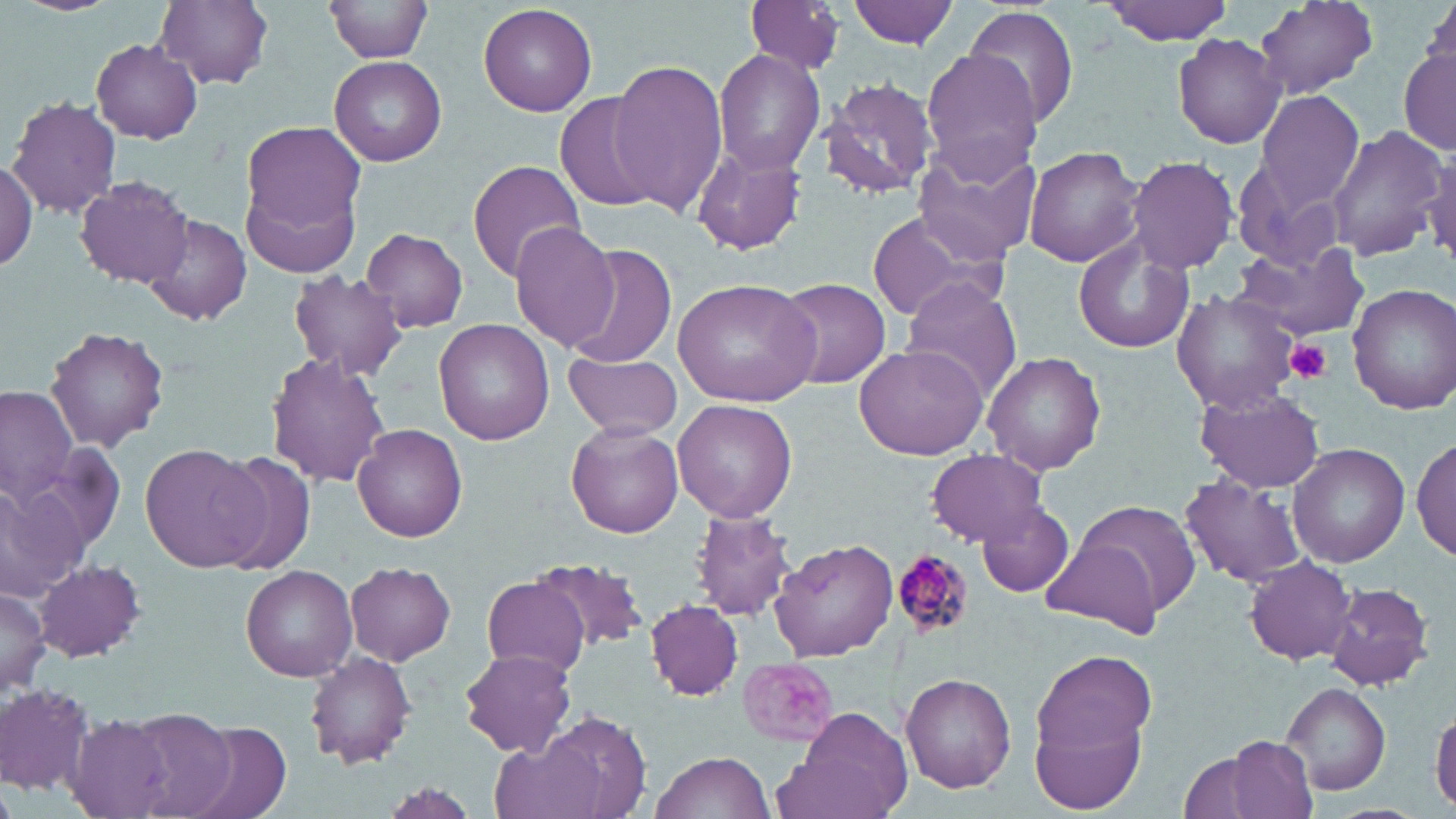
slide-level diagnosis = Plasmodium malariae
magnification = 1000x
preparation = thin blood smear
modality = optical microscopy
field of view = single
platelet locations = approximate bounding boxes as (x1,y1)-(x2,y2) corner pairs in pixels: (1286,339)-(1330,383)
image size = 1456×819 pixels
uninfected red blood cell locations = approximate bounding boxes as (x1,y1)-(x2,y2) corner pairs in pixels: (154,0)-(275,89), (325,0)-(432,63), (848,0)-(958,47), (1101,0)-(1239,44), (1252,0)-(1378,99), (1420,0)-(1456,90), (742,2)-(845,75), (479,3)-(598,116), (963,5)-(1080,130), (1172,34)-(1285,148), (90,39)-(203,143), (1399,47)-(1455,156), (712,49)-(826,176), (921,49)-(1044,180), (329,56)-(447,165), (608,60)-(727,214), (822,77)-(938,199), (1256,89)-(1366,210), (554,91)-(663,214), (7,96)-(121,219), (1327,124)-(1446,261), (239,125)-(365,275), (691,143)-(808,256), (1024,144)-(1145,267), (1422,144)-(1456,269), (911,147)-(1041,267), (1126,155)-(1239,274), (0,158)-(37,271), (468,159)-(586,282), (75,175)-(194,287), (864,211)-(1006,325), (144,213)-(251,326), (508,222)-(621,352), (362,227)-(467,332), (1072,239)-(1195,354), (1233,241)-(1371,342), (568,246)-(676,368), (288,269)-(406,382), (672,278)-(820,407), (771,278)-(891,390), (899,279)-(1022,400), (1348,283)-(1456,414), (1171,289)-(1300,414), (434,318)-(556,444), (45,324)-(169,451), (855,344)-(988,460), (565,350)-(684,442), (984,351)-(1106,475), (266,353)-(390,488), (1,386)-(76,510), (1197,389)-(1324,493), (674,399)-(797,521), (565,422)-(683,538), (353,423)-(467,544), (1412,436)-(1455,561), (141,442)-(265,571), (1288,444)-(1409,568), (925,451)-(1048,546), (209,452)-(319,571), (1180,471)-(1311,587), (0,474)-(89,606), (1074,498)-(1201,621), (977,500)-(1075,597), (689,509)-(797,623), (1040,538)-(1163,639), (769,539)-(898,662), (1245,556)-(1356,663), (533,558)-(654,655), (35,559)-(145,662), (346,563)-(454,665), (239,566)-(357,681), (482,575)-(591,674), (1324,581)-(1435,691), (0,585)-(51,697), (647,600)-(743,701), (461,649)-(578,756), (305,651)-(418,768), (1032,652)-(1159,764), (898,672)-(1016,792), (0,679)-(96,797), (1283,682)-(1391,795), (1030,688)-(1150,815), (787,693)-(1019,807), (775,705)-(915,819), (1431,706)-(1456,812), (116,708)-(237,819), (515,714)-(653,817), (67,717)-(175,817), (170,718)-(293,819), (1225,736)-(1318,819), (1174,749)-(1274,819), (649,750)-(779,819)
stain = May-Grünwald-Giemsa
Plasmodium malariae-infected red blood cell locations = approximate bounding boxes as (x1,y1)-(x2,y2) corner pairs in pixels: (891,548)-(973,641)